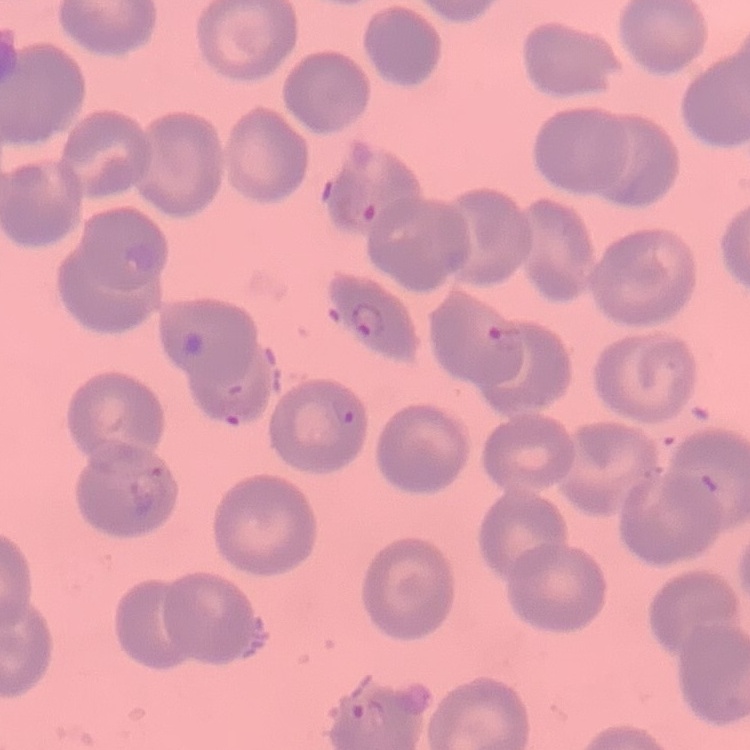
erythrocyte morphology = no rouleaux formation
stain = Field's or Giemsa
image type = square crop of a larger photomicrograph
preparation = thin blood film